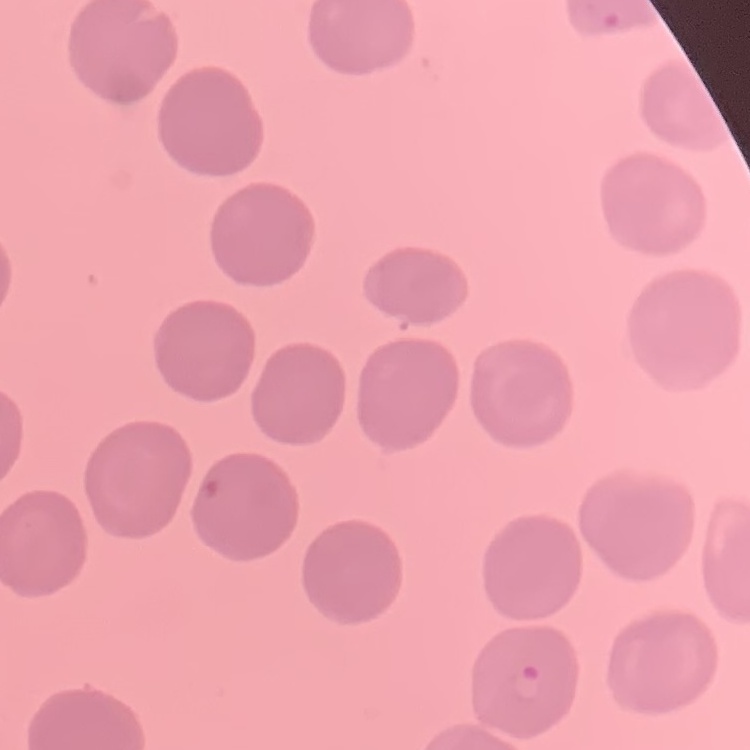

Summary:
  - Erythrocyte morphology: no rouleaux formation
  - Stain: Field's or Giemsa
  - Preparation: thin blood smear
  - Image type: square crop of a larger photomicrograph